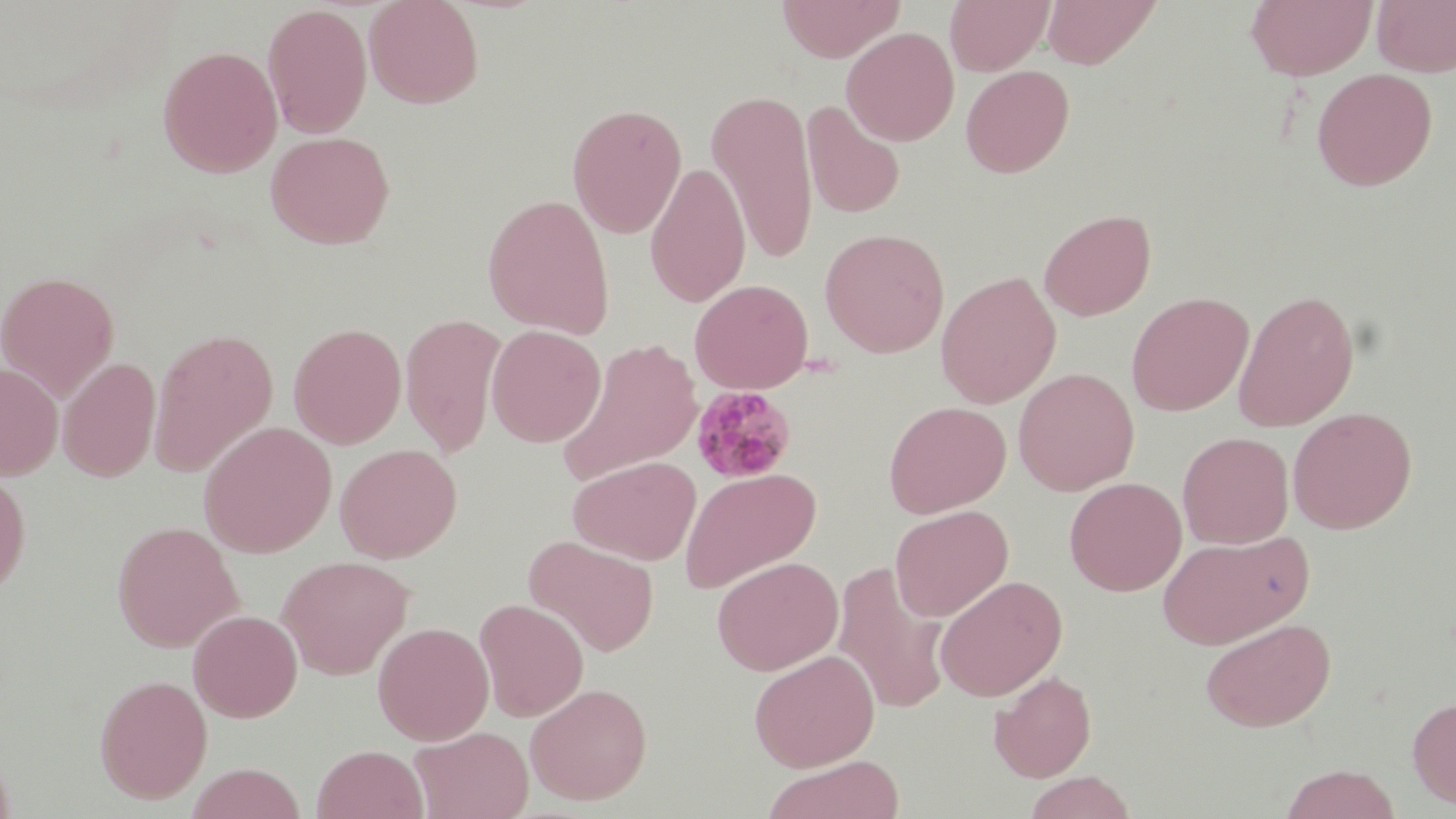
Summary:
  - Coordinate format: approximate bounding boxes as named x1/y1/x2/y2 corners in pixels
  - Plasmodium malariae-infected red blood cell locations: (x1=688, y1=385, x2=797, y2=485)
  - Uninfected red blood cell locations: (x1=364, y1=0, x2=484, y2=108), (x1=776, y1=0, x2=904, y2=62), (x1=945, y1=0, x2=1053, y2=75), (x1=1042, y1=0, x2=1162, y2=69), (x1=1246, y1=0, x2=1376, y2=81), (x1=1372, y1=0, x2=1456, y2=77), (x1=262, y1=4, x2=372, y2=138), (x1=841, y1=26, x2=959, y2=146), (x1=158, y1=45, x2=283, y2=177), (x1=960, y1=64, x2=1075, y2=178), (x1=1311, y1=67, x2=1438, y2=191), (x1=707, y1=89, x2=819, y2=266), (x1=801, y1=101, x2=905, y2=220), (x1=567, y1=102, x2=687, y2=237), (x1=265, y1=130, x2=395, y2=249), (x1=645, y1=162, x2=751, y2=307), (x1=482, y1=193, x2=615, y2=339), (x1=1039, y1=208, x2=1156, y2=321), (x1=819, y1=227, x2=950, y2=357), (x1=0, y1=270, x2=119, y2=400), (x1=936, y1=270, x2=1062, y2=409), (x1=690, y1=278, x2=813, y2=394), (x1=1233, y1=288, x2=1360, y2=432), (x1=1126, y1=291, x2=1253, y2=416), (x1=400, y1=313, x2=506, y2=457), (x1=288, y1=322, x2=407, y2=449), (x1=486, y1=324, x2=605, y2=447), (x1=148, y1=327, x2=278, y2=478), (x1=556, y1=337, x2=704, y2=484), (x1=58, y1=357, x2=160, y2=482), (x1=0, y1=362, x2=63, y2=480), (x1=1013, y1=367, x2=1139, y2=496), (x1=883, y1=400, x2=1011, y2=518), (x1=1288, y1=407, x2=1417, y2=534), (x1=199, y1=421, x2=337, y2=558), (x1=1177, y1=430, x2=1294, y2=549), (x1=335, y1=443, x2=462, y2=563), (x1=568, y1=455, x2=701, y2=565), (x1=679, y1=467, x2=822, y2=593), (x1=0, y1=469, x2=31, y2=599), (x1=1064, y1=476, x2=1186, y2=596), (x1=889, y1=505, x2=1013, y2=622), (x1=112, y1=520, x2=243, y2=653), (x1=1156, y1=529, x2=1312, y2=649), (x1=523, y1=535, x2=660, y2=657), (x1=277, y1=555, x2=413, y2=680), (x1=711, y1=556, x2=843, y2=675), (x1=832, y1=561, x2=950, y2=715), (x1=934, y1=574, x2=1068, y2=701), (x1=475, y1=598, x2=589, y2=722), (x1=188, y1=609, x2=302, y2=722), (x1=1200, y1=617, x2=1336, y2=732), (x1=372, y1=621, x2=494, y2=745), (x1=748, y1=649, x2=879, y2=771), (x1=989, y1=670, x2=1096, y2=783), (x1=94, y1=673, x2=213, y2=804), (x1=525, y1=682, x2=652, y2=806), (x1=1407, y1=695, x2=1456, y2=809), (x1=409, y1=725, x2=533, y2=819), (x1=312, y1=745, x2=427, y2=819), (x1=762, y1=755, x2=906, y2=819), (x1=186, y1=762, x2=307, y2=819), (x1=1279, y1=763, x2=1402, y2=819), (x1=1022, y1=771, x2=1138, y2=818)
  - Slide-level diagnosis: Plasmodium malariae
  - Image size: 1456×819 pixels
  - Field of view: one of a larger specimen
  - Preparation: thin blood smear
  - Modality: light microscopy
  - Stain: May-Grünwald-Giemsa
  - Magnification: 1000x